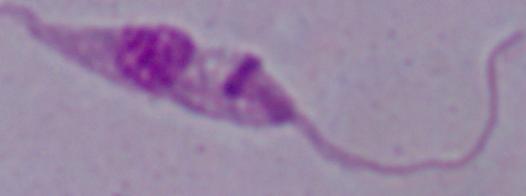

modality = micrograph
identification = Leishmania
magnification = 1000x